State the preparation type.
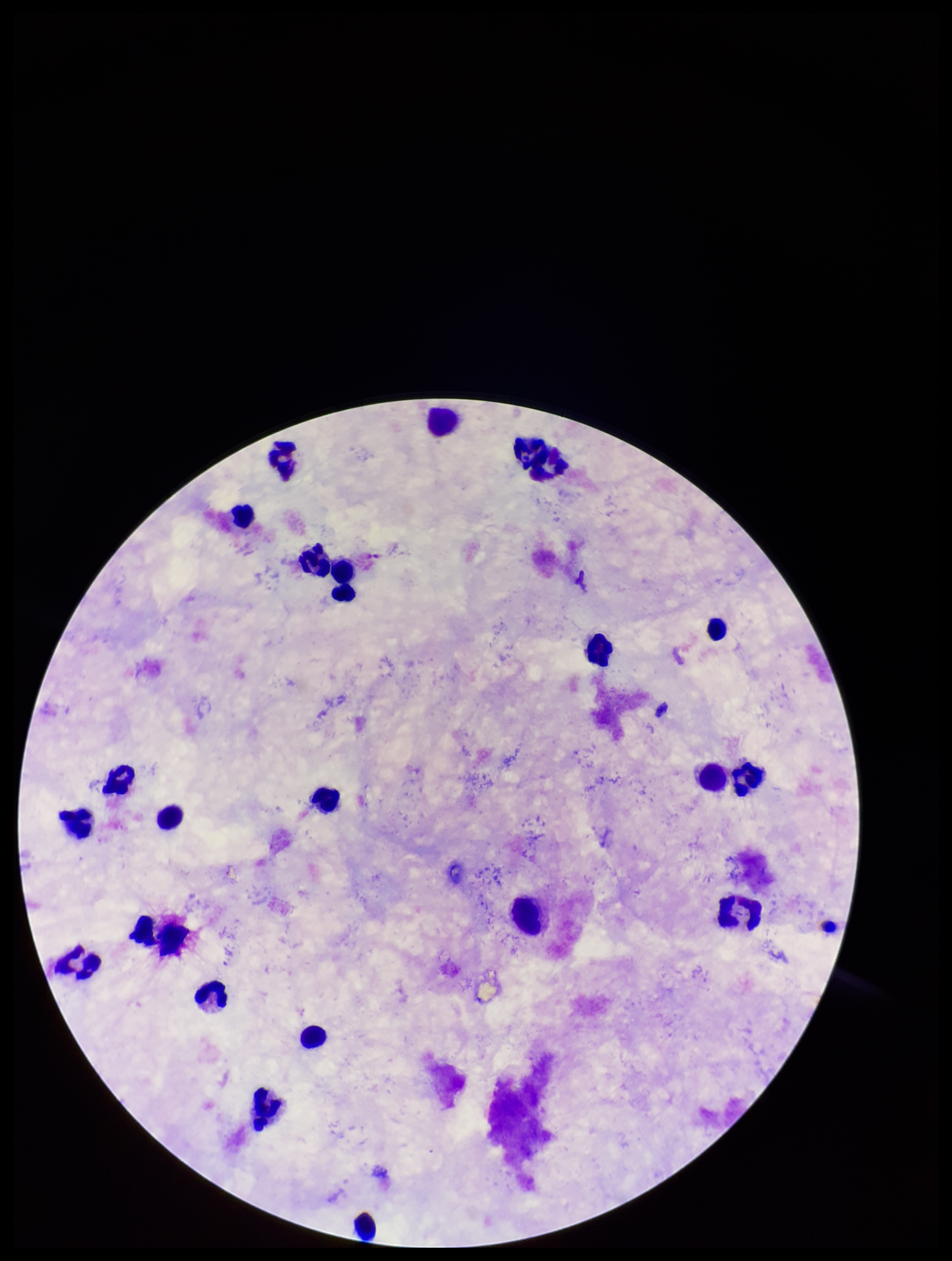
Thick.

Patient malaria status: negative. Giemsa stain. Parasite count: 0. Plasmodium parasites: none detected. Single field of view. Image is 952×1261 pixels. Smartphone photograph taken through the eyepiece of a microscope. Leukocyte count: 25.